Point out each Plasmodium parasite.
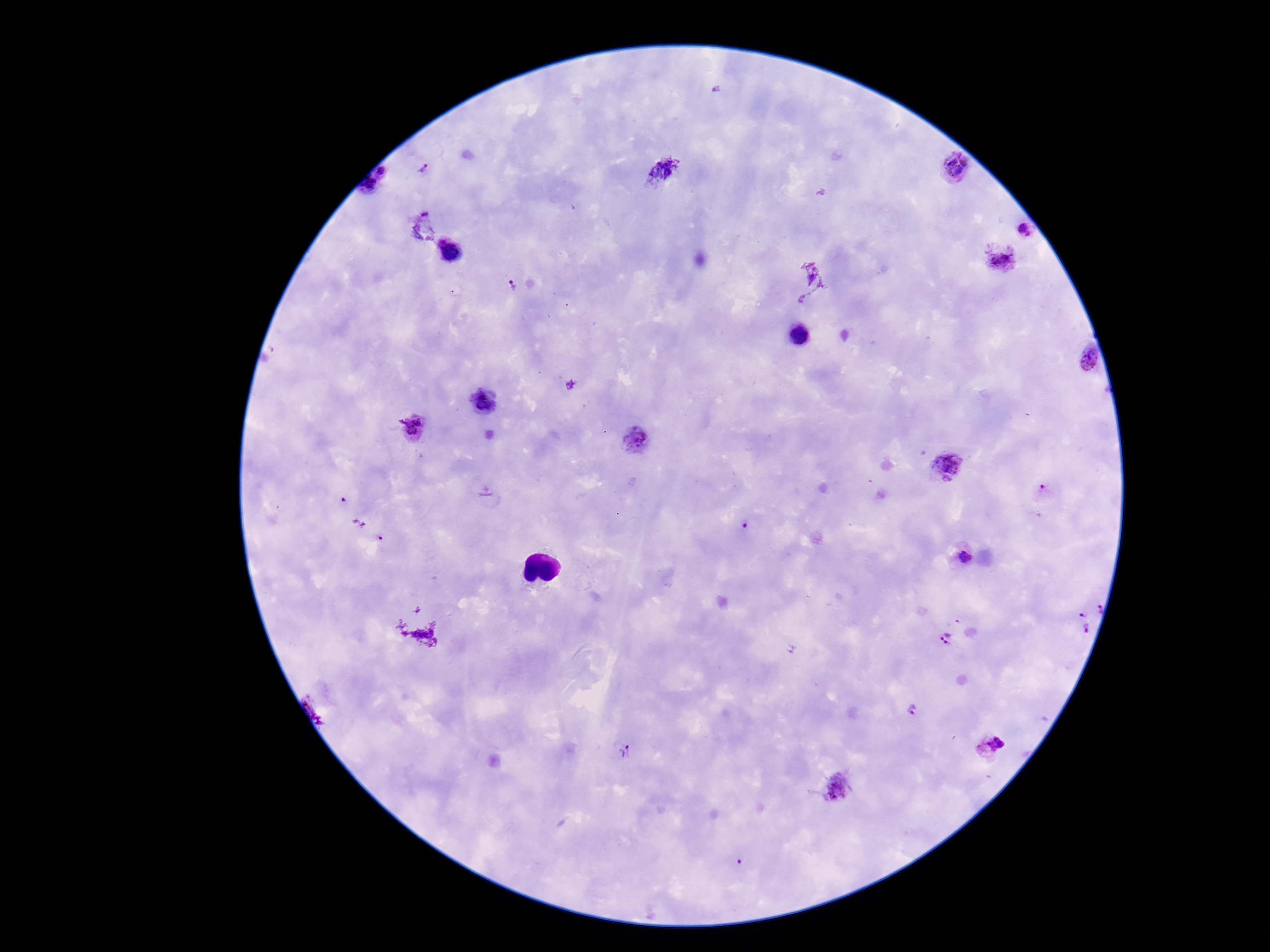
Approximate centers as {x, y} in pixels.
Plasmodium parasites: {425, 170}, {954, 171}, {1025, 233}, {448, 252}, {1000, 261}, {810, 280}, {514, 288}, {1085, 361}, {483, 404}, {414, 428}, {635, 439}, {949, 466}, {344, 502}, {745, 525}, {380, 539}, {961, 557}, {1098, 603}, {1080, 626}, {947, 639}, {913, 711}, {988, 746}, {623, 755}, {741, 863}.

100x magnification. Image is 1270×952 pixels. One field from this slide. Giemsa-stained preparation. Thick peripheral-blood smear. Patient malaria status: positive. Photographed through the microscope eyepiece with a smartphone camera.